Give the extent of all Plasmodium vivax-infected red blood cells.
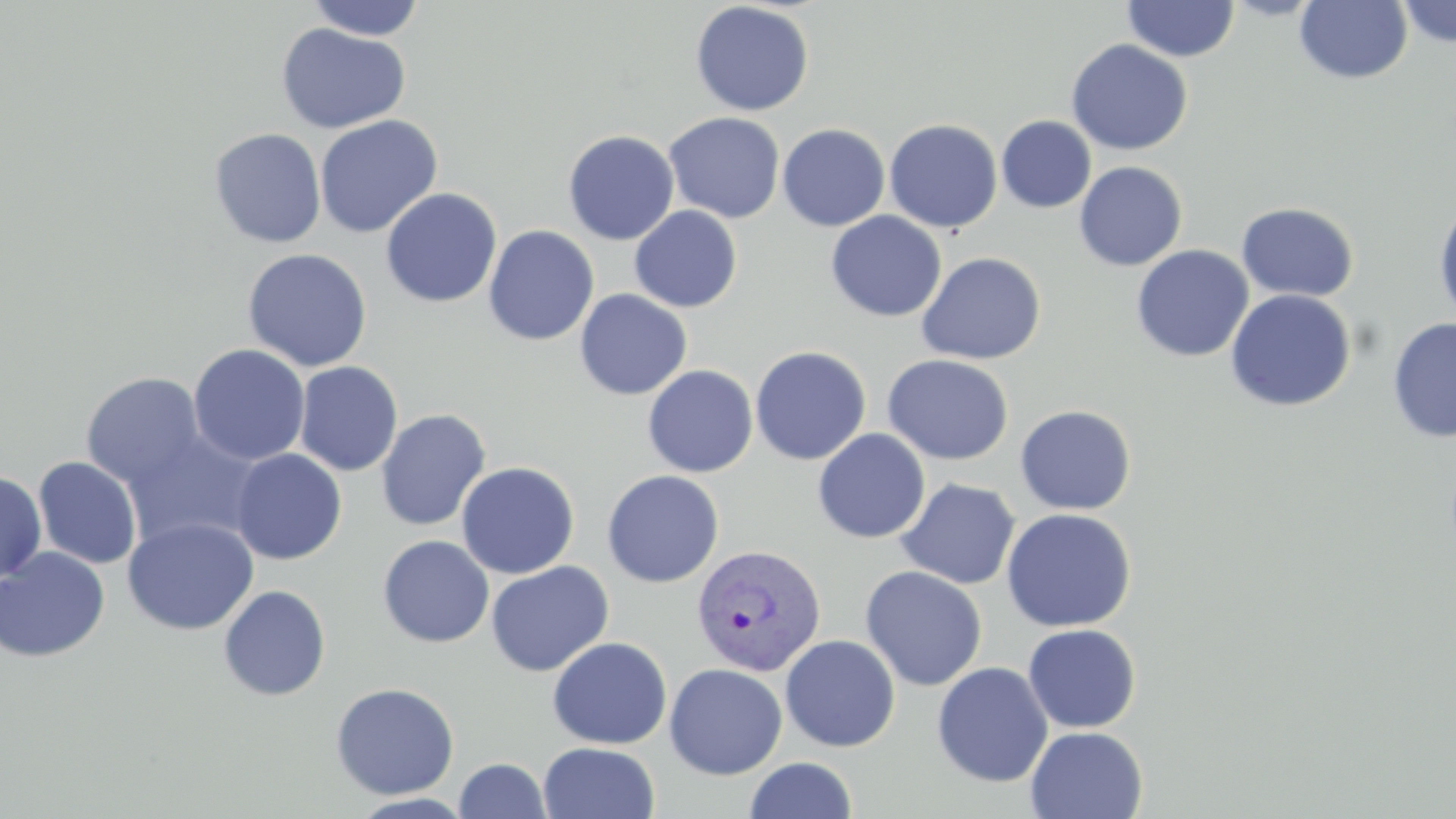

Approximate bounding boxes as [x1, y1, x2, y2] in pixels.
Plasmodium vivax-infected red blood cells: [692, 543, 827, 675].

Summary:
  - Uninfected red blood cell locations: [305, 0, 426, 40], [1221, 0, 1325, 20], [1396, 0, 1456, 48], [690, 1, 814, 116], [1122, 1, 1239, 62], [1294, 1, 1413, 85], [276, 23, 411, 135], [1066, 39, 1193, 156], [664, 112, 786, 224], [314, 114, 443, 238], [997, 115, 1096, 213], [883, 119, 1003, 233], [777, 123, 890, 231], [208, 128, 327, 248], [562, 129, 680, 245], [1074, 161, 1188, 271], [380, 188, 502, 309], [1432, 198, 1456, 325], [1236, 202, 1359, 303], [629, 206, 742, 312], [826, 210, 947, 322], [482, 225, 600, 346], [1131, 244, 1254, 362], [242, 248, 372, 372], [916, 251, 1047, 365], [574, 289, 692, 400], [1224, 289, 1357, 412], [1387, 316, 1456, 443], [188, 344, 311, 466], [749, 346, 872, 465], [882, 354, 1014, 465], [294, 361, 403, 477], [643, 365, 758, 478], [81, 371, 207, 489], [1014, 404, 1137, 515], [376, 408, 492, 531], [120, 428, 265, 551], [812, 428, 931, 543], [230, 449, 347, 565], [33, 456, 142, 569], [456, 461, 580, 579], [0, 470, 46, 583], [602, 470, 724, 588], [896, 478, 1021, 589], [1000, 507, 1137, 632], [123, 517, 259, 635], [377, 536, 495, 647], [0, 546, 110, 663], [485, 561, 614, 677], [859, 565, 987, 691], [218, 585, 332, 701], [1022, 623, 1141, 733], [780, 635, 900, 752], [547, 636, 673, 749], [932, 661, 1053, 788], [664, 663, 788, 779], [330, 681, 460, 800], [1025, 726, 1148, 818], [539, 742, 660, 819], [744, 757, 858, 818], [454, 758, 552, 818]
  - Slide-level diagnosis: Plasmodium vivax
  - Field of view: one of a larger specimen
  - Image size: 1456×819 pixels
  - Modality: light microscopy
  - Stain: May-Grünwald-Giemsa
  - Magnification: 1000x
  - Preparation: thin blood smear